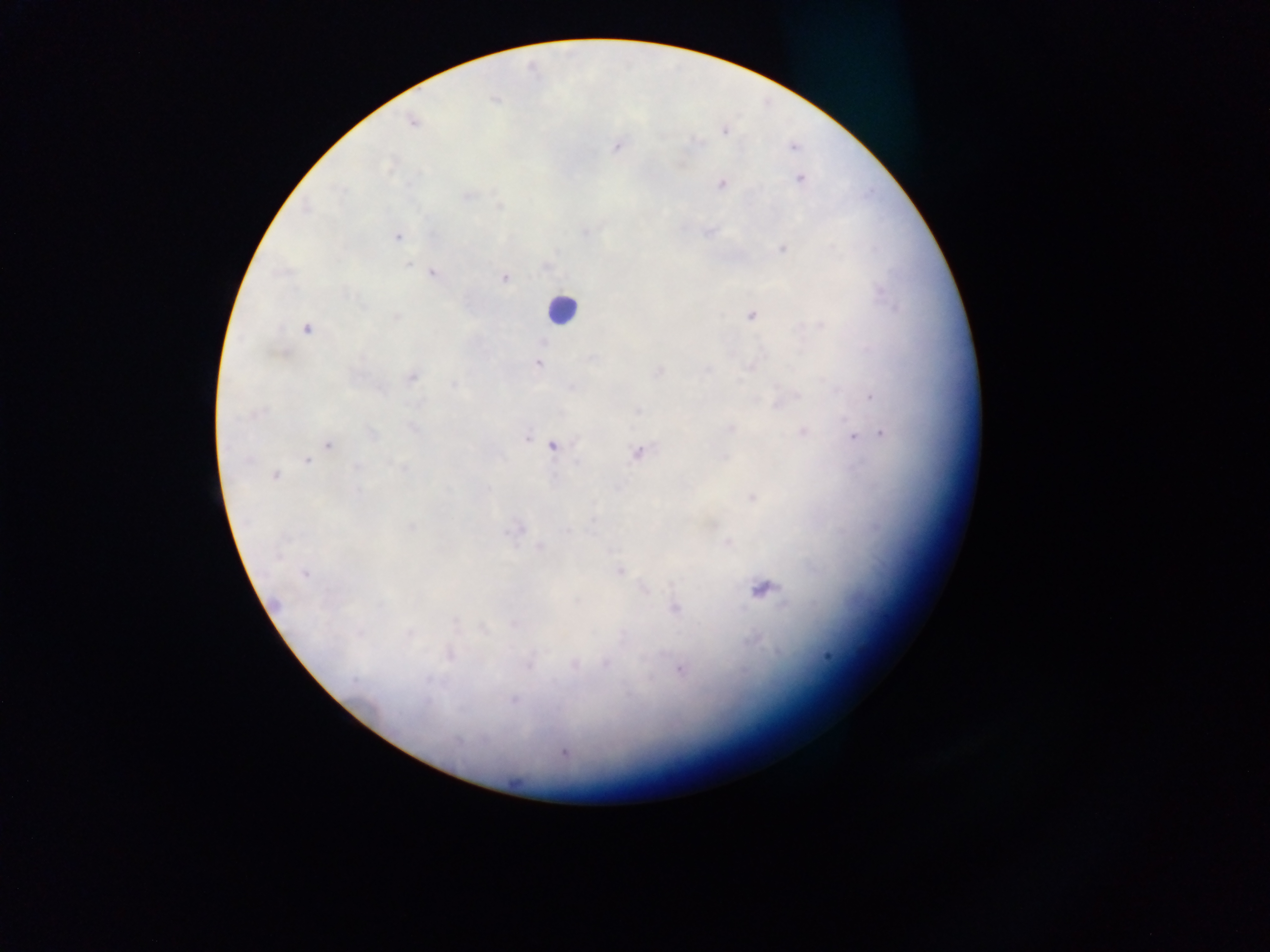

malaria parasite locations = approximate centers as x y in pixels: 495 100; 411 122; 725 131; 617 146; 793 147; 800 178; 721 184; 467 196; 500 206; 585 232; 709 232; 398 237; 782 249; 408 264; 432 273; 504 277; 751 316; 396 317; 821 326; 306 328; 544 341; 537 364; 750 366; 708 369; 659 371; 411 377; 454 384; 798 396; 872 396; 777 406; 638 411; 730 428; 414 429; 802 431; 371 434; 883 434; 526 437; 853 438; 329 445; 552 447; 638 453; 725 458; 248 460; 307 461; 356 466; 403 468; 275 476; 358 490; 752 497; 713 524; 411 526; 517 529; 566 531; 540 547; 279 555; 620 572; 304 574; 763 589; 645 590; 675 609; 456 621; 483 629; 359 634; 409 634; 623 636; 450 655; 828 656; 606 664; 528 665; 575 666; 680 670; 432 679; 355 681; 514 700; 427 701; 458 741; 564 753
leukocyte locations = approximate centers as x y in pixels: 561 309
preparation = thick blood smear
country = Ghana
image size = 1270×952 pixels
field of view = single
capture = mobile-phone photograph through a microscope